Classify this cell by malaria status.
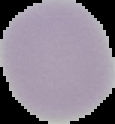

Uninfected.

The area outside the segmented cell region is set to black. Image is 115×124 pixels. From a thin blood smear.